Give a bounding box for every malaria parasite.
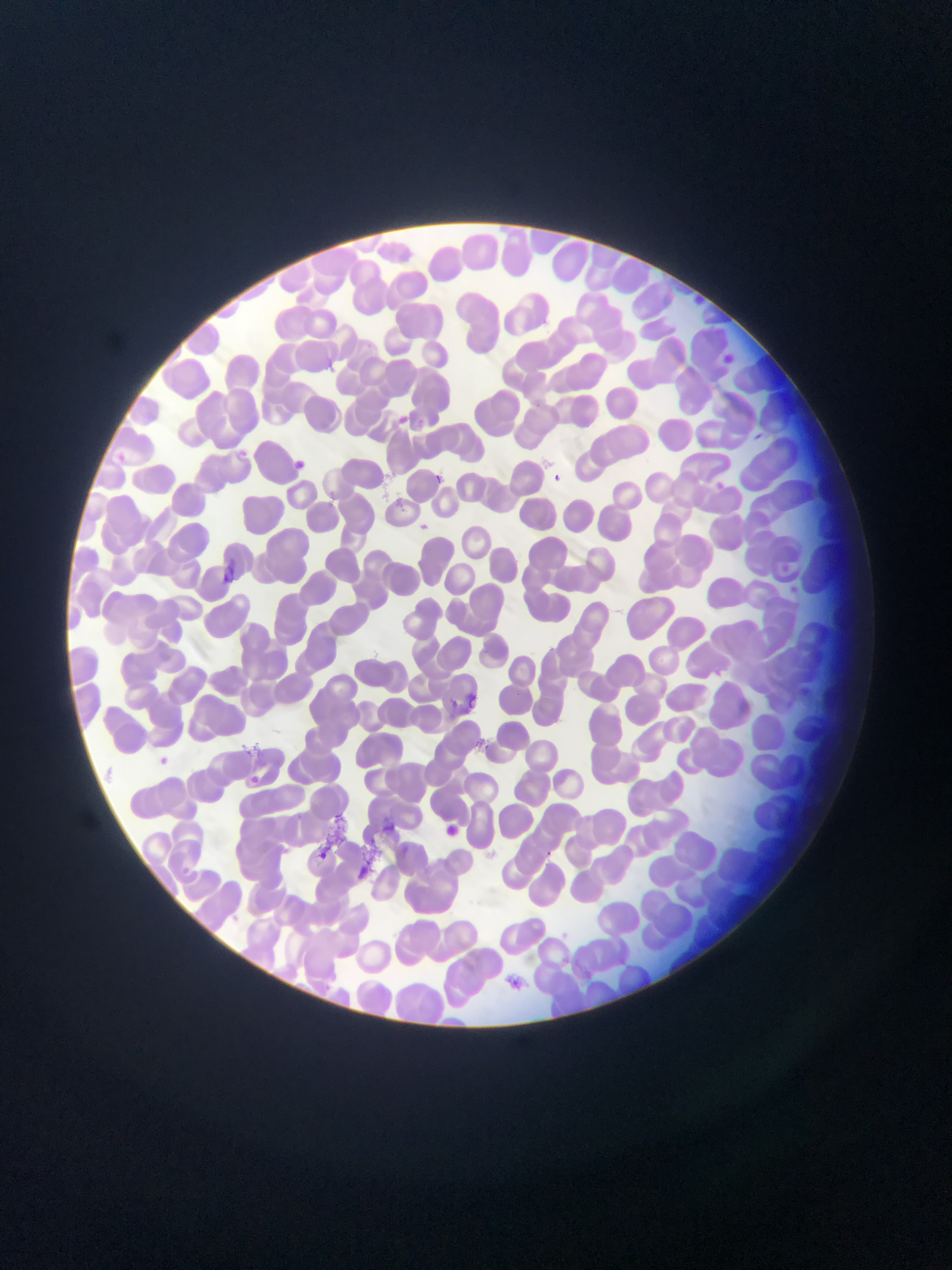
Approximate bounding boxes as (left, top, right, bottom) in pixels.
Malaria parasites: (718, 352, 740, 372), (322, 357, 337, 371), (317, 360, 338, 378), (393, 413, 410, 428), (236, 445, 248, 456), (290, 459, 315, 473), (545, 471, 564, 489), (430, 472, 445, 487), (711, 479, 728, 494), (416, 521, 432, 535), (153, 752, 174, 771), (246, 772, 263, 788), (438, 821, 462, 841), (315, 848, 331, 864), (543, 850, 556, 860), (504, 974, 525, 992).

Summary:
  - Artifact (stain precipitate or debris) locations: (222, 553, 239, 582), (464, 687, 484, 714), (318, 812, 352, 846), (355, 839, 389, 876)
  - Image size: 952×1270 pixels
  - Capture: mobile-phone photograph through a microscope
  - Country: Ghana
  - Preparation: thin blood film
  - Field of view: single